Name the blood parasite species.
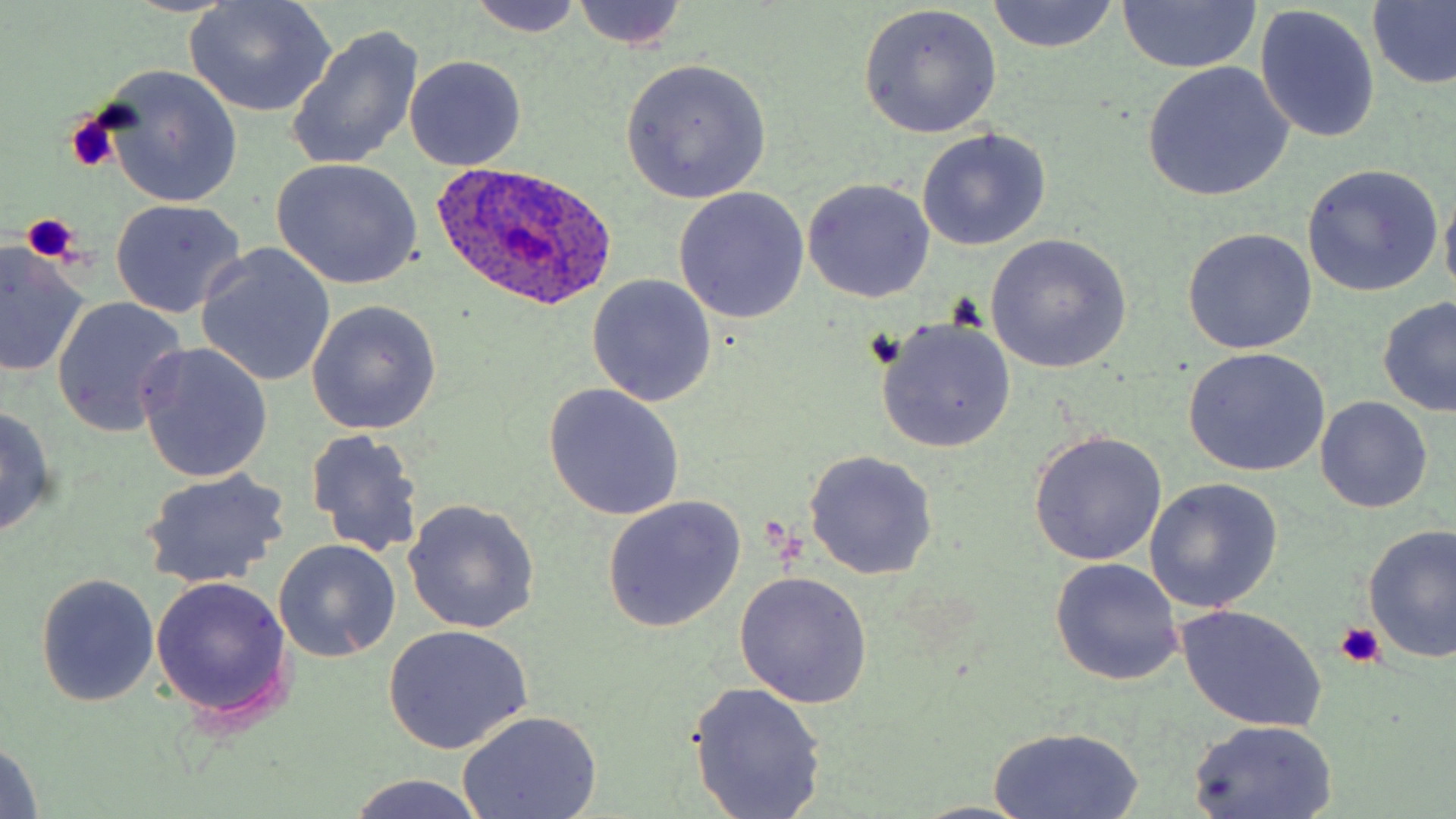

Plasmodium ovale.

Summary:
  - Coordinate format: approximate bounding boxes as (x1, y1, x2, y2) in pixels
  - Plasmodium ovale-infected red blood cell locations: (433, 159, 618, 309)
  - Platelet locations: (66, 111, 121, 175), (21, 211, 82, 265), (860, 328, 906, 371), (1333, 620, 1386, 670)
  - Uninfected red blood cell locations: (182, 0, 334, 117), (463, 0, 586, 37), (569, 1, 689, 51), (989, 1, 1119, 54), (1116, 2, 1261, 73), (1366, 2, 1456, 91), (859, 5, 1001, 139), (1255, 6, 1380, 144), (286, 25, 424, 171), (404, 55, 527, 171), (620, 59, 772, 202), (1142, 62, 1293, 200), (97, 65, 244, 210), (916, 128, 1050, 251), (271, 159, 422, 290), (1303, 164, 1442, 295), (803, 178, 935, 303), (672, 187, 810, 325), (1441, 187, 1456, 307), (109, 198, 245, 318), (1183, 229, 1317, 355), (986, 235, 1133, 374), (0, 243, 89, 375), (195, 245, 336, 387), (587, 275, 717, 408), (1377, 297, 1456, 418), (50, 298, 187, 436), (305, 301, 442, 435), (875, 317, 1017, 454), (137, 343, 272, 482), (1182, 347, 1330, 476), (543, 385, 684, 520), (1315, 396, 1432, 512), (0, 405, 58, 541), (306, 428, 424, 558), (1028, 430, 1167, 566), (802, 449, 939, 581), (140, 470, 290, 589), (1144, 479, 1281, 613), (604, 495, 744, 633), (403, 498, 539, 634), (1362, 525, 1456, 663), (273, 539, 401, 663), (1050, 558, 1184, 686), (734, 571, 873, 708), (35, 573, 159, 707), (151, 576, 294, 725), (1176, 606, 1327, 732), (382, 625, 534, 755), (689, 682, 826, 818), (456, 710, 604, 819), (1188, 718, 1341, 818), (986, 725, 1145, 819), (1, 738, 44, 817), (347, 774, 488, 819), (912, 801, 1035, 818)
  - Field of view: single
  - Preparation: thin blood smear
  - Modality: light microscopy
  - Image size: 1456×819 pixels
  - Stain: May-Grünwald-Giemsa
  - Magnification: 1000x